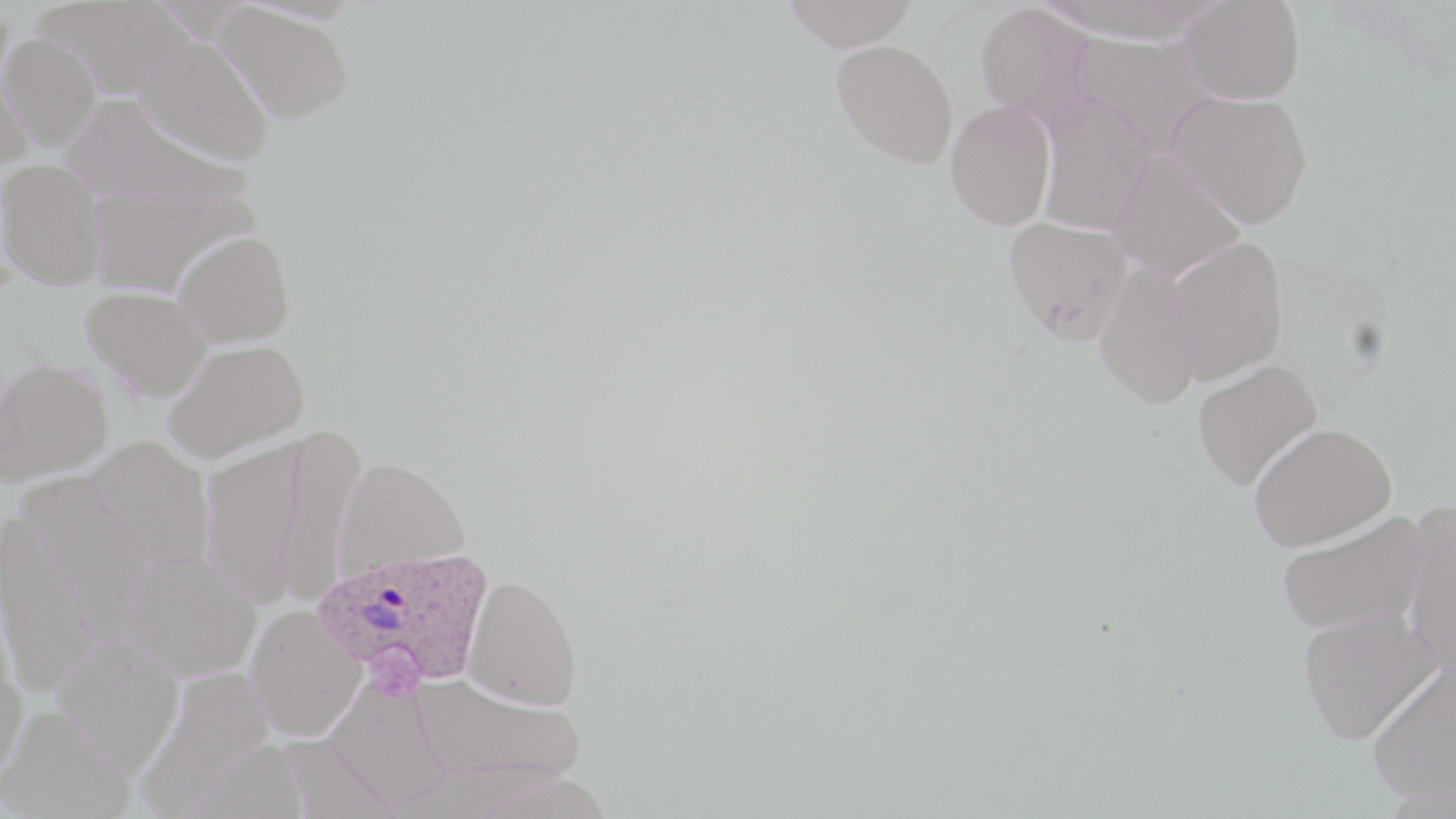

Approximate bounding boxes as (x1, y1, x2, y2) in pixels. Plasmodium ovale-infected red blood cell locations: (314, 544, 495, 691). Uninfected red blood cell locations: (780, 0, 918, 51), (1036, 0, 1225, 45), (1179, 0, 1305, 104), (215, 2, 354, 123), (974, 2, 1097, 127), (1, 31, 102, 152), (1075, 31, 1222, 155), (135, 36, 274, 166), (831, 39, 958, 168), (0, 53, 34, 170), (1167, 91, 1314, 228), (58, 93, 246, 208), (1036, 93, 1156, 235), (945, 99, 1056, 230), (1107, 149, 1246, 282), (0, 159, 106, 290), (85, 187, 260, 297), (1003, 215, 1133, 343), (172, 229, 296, 348), (1170, 235, 1289, 385), (1094, 260, 1199, 409), (82, 286, 213, 400), (163, 340, 308, 462), (0, 358, 113, 485), (1191, 358, 1323, 490), (1249, 422, 1397, 550), (272, 425, 366, 608), (86, 437, 214, 572), (199, 438, 307, 609), (333, 456, 469, 578), (17, 475, 155, 635), (1400, 500, 1456, 681), (1276, 510, 1427, 635), (0, 513, 100, 696), (120, 550, 260, 682), (462, 573, 583, 709), (245, 604, 365, 742), (1298, 609, 1442, 743), (50, 635, 184, 776), (0, 655, 26, 789), (1366, 661, 1456, 804), (135, 665, 275, 818), (410, 674, 585, 788), (324, 677, 455, 813), (1, 706, 133, 819). Slide-level diagnosis: Plasmodium ovale. 1000x magnification. Thin blood film. One field of a larger specimen. May-Grünwald-Giemsa stain. Light microscopy. Image is 1456×819 pixels.